Locate every leukocyte (white blood cell).
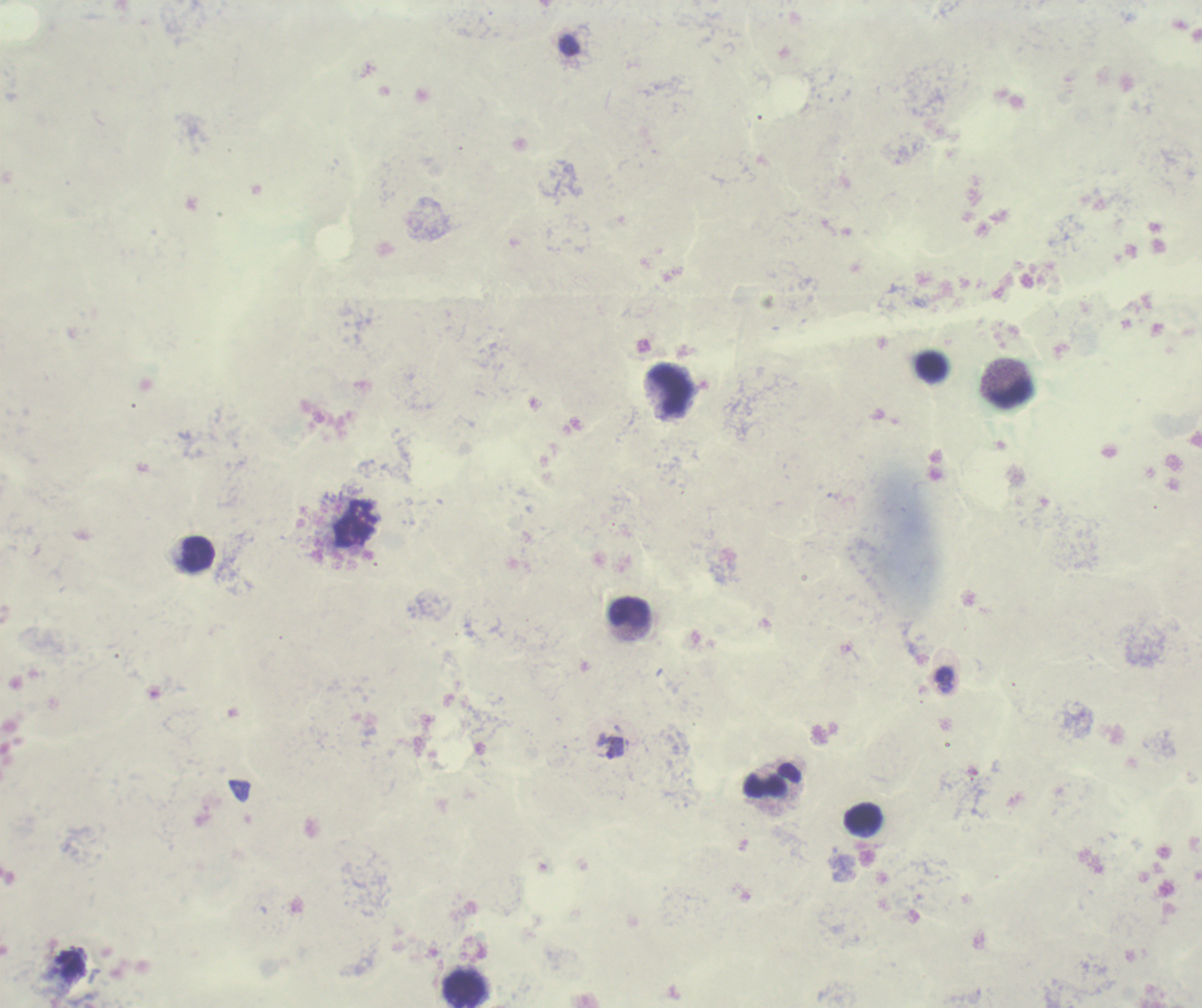
Approximate centers as {x, y} in pixels.
Leukocytes: {672, 390}, {1012, 393}, {195, 554}, {630, 612}, {772, 782}, {864, 819}, {463, 989}.

Approximate centers as {x, y} in pixels.
Summary:
  - Trophozoite locations: {614, 748}
  - Context: previously used in an actual diagnosis
  - Coloration quality: bad
  - Result: positive for Plasmodium parasites
  - Image size: 1202×1008 pixels
  - Background quality: poor
  - Preparation: thick blood film
  - Field of view: single
  - Stain: Romanowsky
  - Magnification: 100x